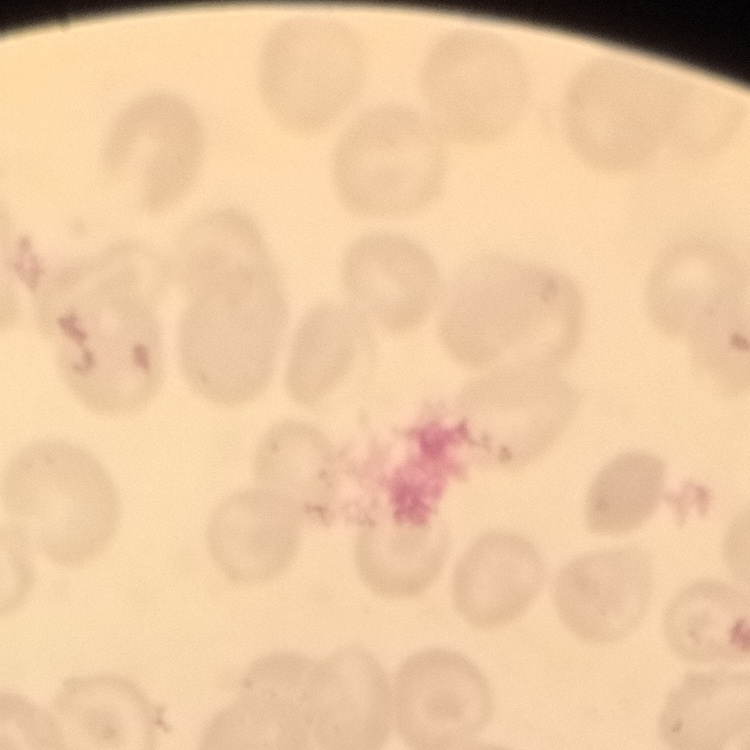

The red blood cells exhibit no rouleaux formation. Field's or Giemsa stain. Square crop of a larger photomicrograph. Thin blood smear.